Report the malaria status of this cell.
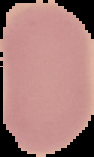
Uninfected.

{
  "image_size": "94×157 pixels",
  "preparation": "thin blood smear",
  "image_type": "segmented cell region with the area outside set to black"
}